Assess this cell for malaria.
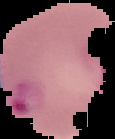

Parasitized.

image_type: segmented cell region on a black background
image_size: 115×139 pixels
preparation: thin blood smear